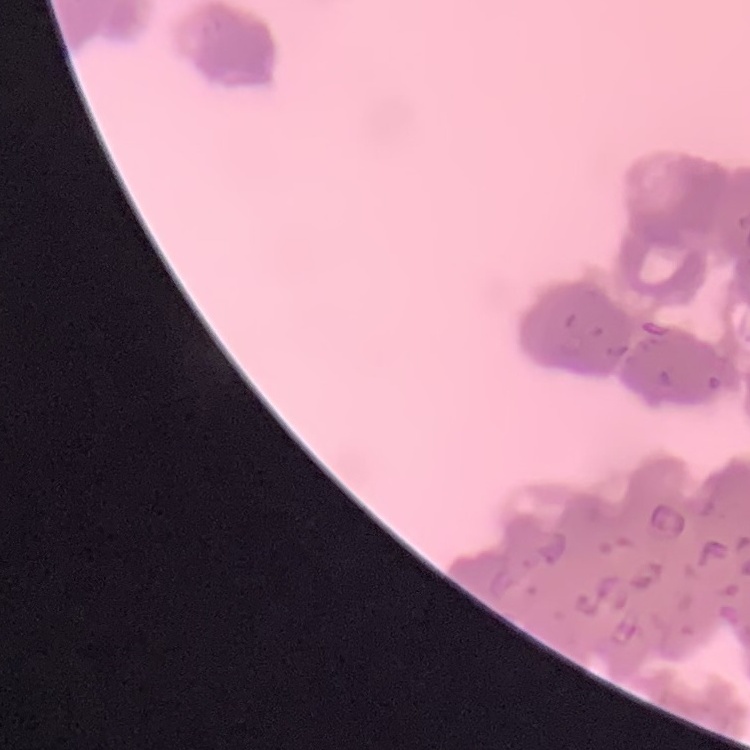

Summary:
  - Red blood cell morphology: rouleaux formation
  - Stain: Field's or Giemsa
  - Image type: square crop of a larger photomicrograph
  - Preparation: thin peripheral smear